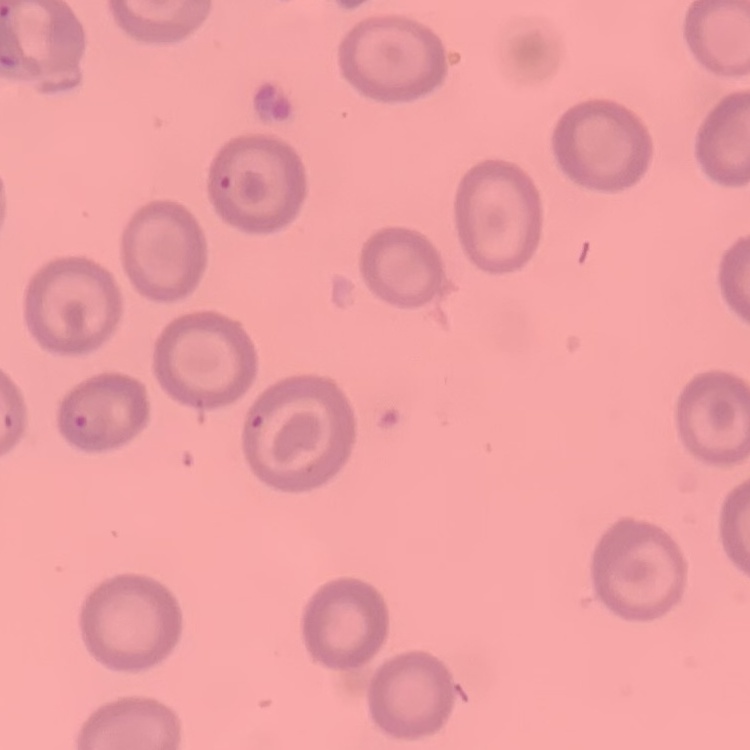

The red blood cells show no rouleaux formation. Square crop of a larger photomicrograph. Thin blood film. Stained with either Field's or Giemsa.